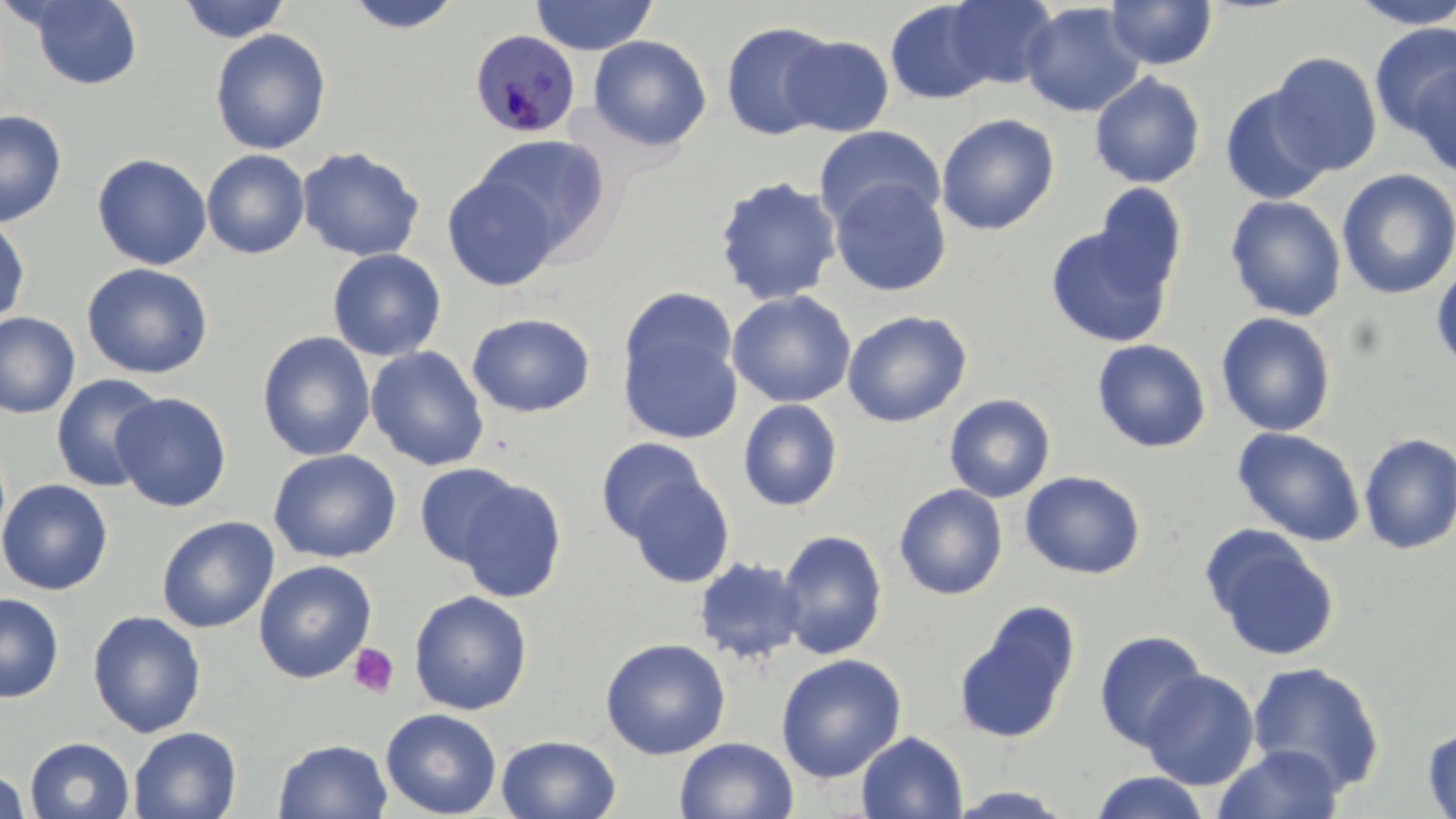 Approximate bounding boxes as named x1/y1/x2/y2 corners in pixels. Plasmodium malariae-infected red blood cell locations: (x1=469, y1=29, x2=580, y2=138). Platelet locations: (x1=347, y1=643, x2=400, y2=698). Uninfected red blood cell locations: (x1=177, y1=0, x2=291, y2=43), (x1=343, y1=0, x2=463, y2=35), (x1=530, y1=0, x2=658, y2=56), (x1=945, y1=0, x2=1058, y2=89), (x1=1105, y1=0, x2=1218, y2=70), (x1=1348, y1=0, x2=1456, y2=29), (x1=24, y1=1, x2=144, y2=90), (x1=885, y1=1, x2=996, y2=105), (x1=1021, y1=2, x2=1145, y2=118), (x1=720, y1=21, x2=838, y2=141), (x1=1369, y1=24, x2=1456, y2=138), (x1=209, y1=28, x2=332, y2=155), (x1=782, y1=34, x2=895, y2=136), (x1=588, y1=35, x2=712, y2=151), (x1=1266, y1=52, x2=1383, y2=177), (x1=1407, y1=65, x2=1455, y2=179), (x1=1088, y1=71, x2=1206, y2=189), (x1=1219, y1=85, x2=1333, y2=205), (x1=0, y1=109, x2=67, y2=227), (x1=936, y1=113, x2=1060, y2=235), (x1=814, y1=125, x2=946, y2=230), (x1=472, y1=133, x2=611, y2=256), (x1=296, y1=146, x2=425, y2=262), (x1=201, y1=149, x2=310, y2=259), (x1=91, y1=153, x2=212, y2=271), (x1=1336, y1=169, x2=1456, y2=299), (x1=442, y1=172, x2=562, y2=291), (x1=713, y1=176, x2=843, y2=306), (x1=828, y1=178, x2=952, y2=297), (x1=1091, y1=183, x2=1188, y2=296), (x1=1224, y1=195, x2=1347, y2=321), (x1=0, y1=217, x2=31, y2=327), (x1=1044, y1=225, x2=1175, y2=348), (x1=327, y1=248, x2=446, y2=361), (x1=81, y1=263, x2=213, y2=378), (x1=1431, y1=263, x2=1456, y2=375), (x1=620, y1=287, x2=739, y2=391), (x1=727, y1=290, x2=856, y2=408), (x1=842, y1=310, x2=973, y2=427), (x1=0, y1=312, x2=81, y2=420), (x1=466, y1=312, x2=595, y2=418), (x1=1215, y1=312, x2=1337, y2=437), (x1=619, y1=326, x2=743, y2=446), (x1=256, y1=331, x2=376, y2=461), (x1=1091, y1=339, x2=1211, y2=453), (x1=365, y1=345, x2=489, y2=471), (x1=50, y1=373, x2=167, y2=492), (x1=111, y1=391, x2=232, y2=512), (x1=943, y1=394, x2=1056, y2=503), (x1=737, y1=398, x2=843, y2=512), (x1=1232, y1=426, x2=1366, y2=546), (x1=1357, y1=432, x2=1456, y2=556), (x1=596, y1=437, x2=708, y2=543), (x1=268, y1=448, x2=402, y2=563), (x1=414, y1=462, x2=527, y2=568), (x1=1020, y1=470, x2=1146, y2=579), (x1=625, y1=473, x2=735, y2=588), (x1=453, y1=477, x2=568, y2=604), (x1=0, y1=478, x2=113, y2=596), (x1=894, y1=483, x2=1008, y2=600), (x1=156, y1=516, x2=280, y2=633), (x1=1201, y1=526, x2=1340, y2=662), (x1=775, y1=529, x2=888, y2=659), (x1=693, y1=557, x2=807, y2=664), (x1=253, y1=559, x2=377, y2=683), (x1=409, y1=590, x2=533, y2=715), (x1=0, y1=592, x2=64, y2=703), (x1=952, y1=601, x2=1080, y2=745), (x1=87, y1=609, x2=207, y2=738), (x1=1093, y1=628, x2=1209, y2=750), (x1=600, y1=637, x2=731, y2=760), (x1=775, y1=653, x2=906, y2=783), (x1=1247, y1=661, x2=1386, y2=794), (x1=1139, y1=669, x2=1260, y2=790), (x1=380, y1=708, x2=502, y2=818), (x1=1422, y1=725, x2=1456, y2=818), (x1=128, y1=726, x2=242, y2=819), (x1=857, y1=731, x2=968, y2=818), (x1=495, y1=734, x2=622, y2=819), (x1=24, y1=736, x2=134, y2=819), (x1=674, y1=736, x2=798, y2=819), (x1=273, y1=738, x2=393, y2=819), (x1=1213, y1=743, x2=1344, y2=819), (x1=0, y1=768, x2=31, y2=818), (x1=1088, y1=770, x2=1212, y2=819), (x1=942, y1=785, x2=1081, y2=818). Slide-level diagnosis: Plasmodium malariae. Image is 1456×819 pixels. One field of a larger specimen. Light microscopy. Captured at 1000x magnification. May-Grünwald-Giemsa stain. Thin blood smear.